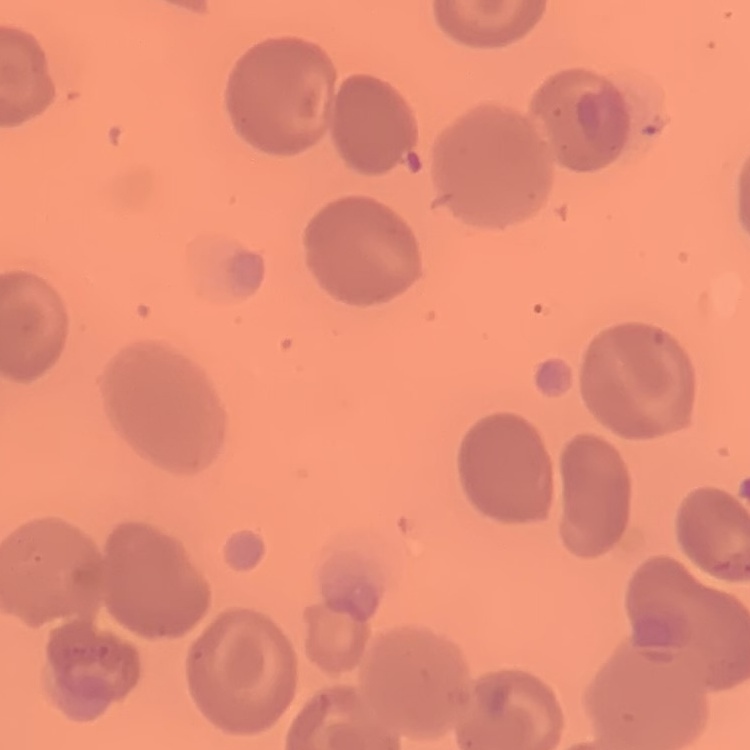

Summary:
  - Red blood cell morphology: no rouleaux formation
  - Stain: Field's or Giemsa
  - Preparation: thin blood smear
  - Image type: one tile cut from a larger photomicrograph